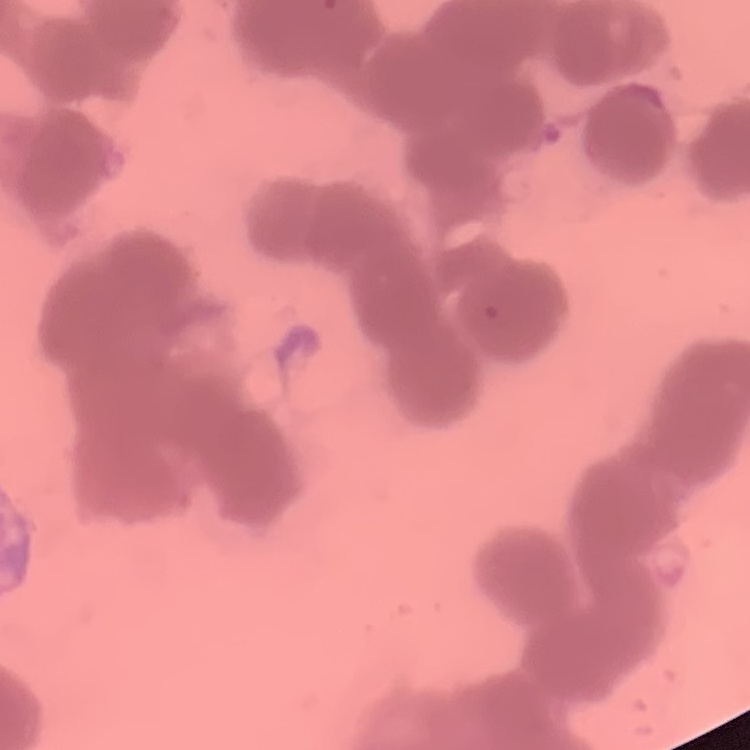

Summary:
  - Erythrocyte morphology: rouleaux formation
  - Image type: one tile cut from a larger photomicrograph
  - Stain: Field's or Giemsa
  - Preparation: thin blood film